Report the malaria status of this cell.
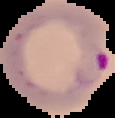

It is parasitized.

Summary:
  - Preparation: thin blood smear
  - Image size: 115×118 pixels
  - Image type: segmented cell region with the area outside set to black